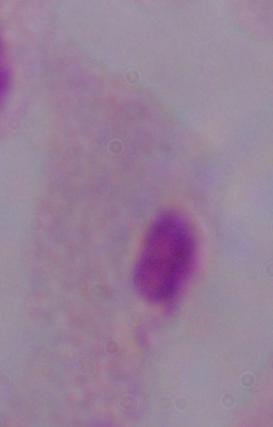

magnification: 1000x
identification: trichomonad
modality: photomicrograph